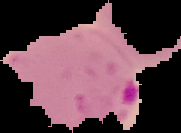 Segmented cell region on a black background. Result: Plasmodium parasites identified. Image is 181×133 pixels. From a thin blood film.